Assess this cell for malaria.
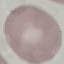
Uninfected.

Summary:
  - Capture: smartphone through the microscope eyepiece
  - Image type: automatically extracted cell patch, resized to 64 × 64 pixels
  - Stain: Giemsa
  - Preparation: thin blood film